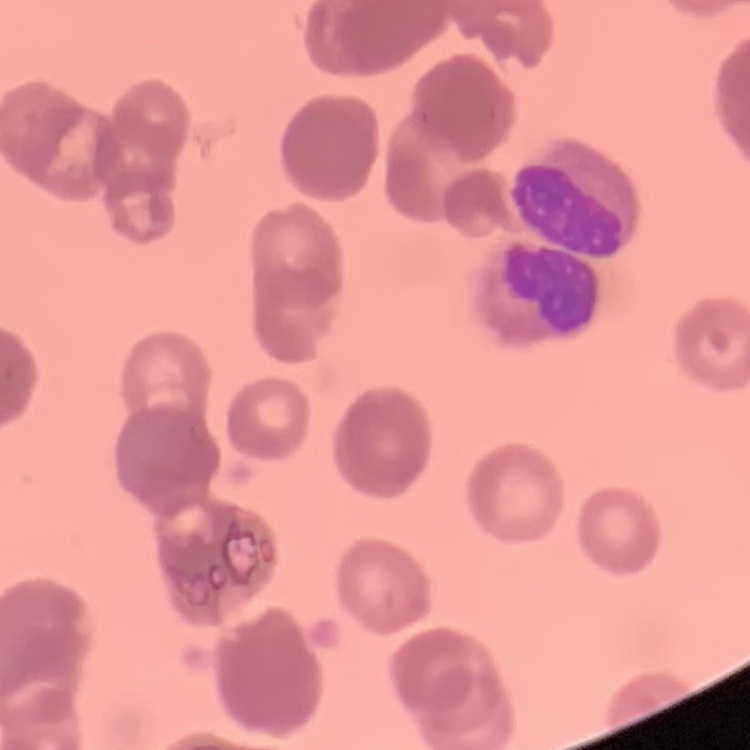 The red blood cells exhibit rouleaux formation. Square crop of a larger photomicrograph. Thin blood smear. Field's or Giemsa stain.